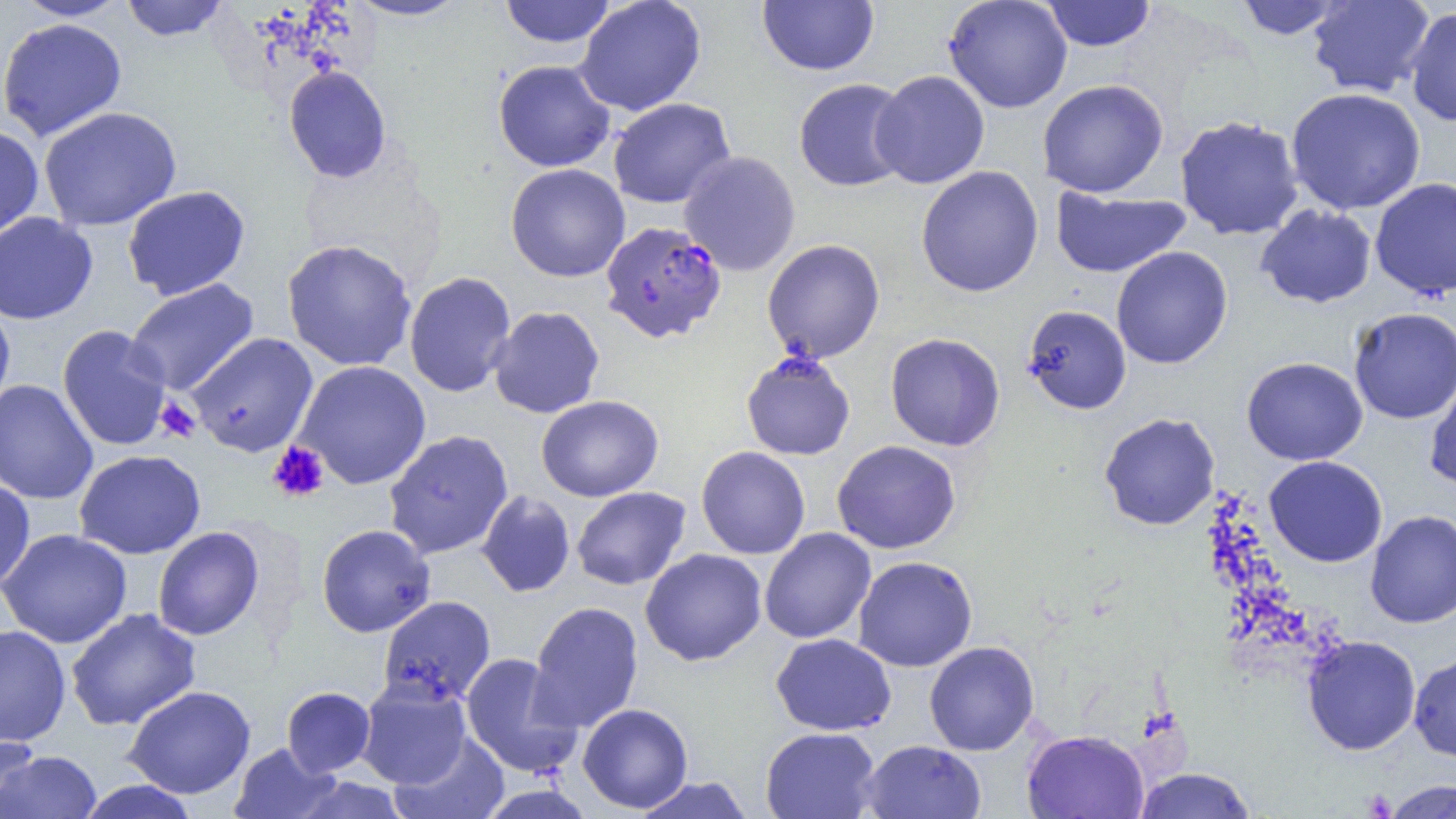

slide-level diagnosis = Plasmodium falciparum
field of view = one of a larger specimen
modality = optical microscopy
Plasmodium falciparum-infected red blood cell locations = approximate bounding boxes as (x1, y1, x2, y2) in pixels: (600, 221, 727, 343)
image size = 1456×819 pixels
platelet locations = approximate bounding boxes as (x1, y1, x2, y2) in pixels: (155, 397, 201, 442), (268, 441, 330, 503), (1361, 788, 1397, 817)
uninfected red blood cell locations = approximate bounding boxes as (x1, y1, x2, y2) in pixels: (12, 0, 132, 21), (119, 0, 231, 42), (345, 0, 471, 21), (499, 0, 618, 48), (575, 0, 706, 116), (943, 0, 1073, 113), (1232, 0, 1349, 40), (1306, 0, 1434, 98), (757, 1, 879, 76), (1041, 1, 1157, 52), (1405, 6, 1456, 127), (0, 17, 127, 142), (492, 59, 616, 172), (284, 65, 391, 183), (871, 70, 990, 189), (793, 78, 912, 192), (1037, 79, 1169, 198), (1286, 88, 1426, 215), (608, 97, 735, 209), (38, 106, 182, 231), (1174, 115, 1305, 241), (0, 125, 45, 242), (678, 151, 801, 276), (505, 163, 630, 282), (915, 166, 1044, 297), (1370, 177, 1456, 300), (122, 185, 251, 300), (1050, 188, 1191, 278), (1255, 204, 1377, 308), (0, 212, 98, 325), (281, 238, 417, 372), (762, 239, 885, 363), (1111, 246, 1233, 369), (403, 271, 517, 398), (124, 278, 260, 397), (1022, 304, 1132, 415), (0, 305, 15, 413), (488, 306, 605, 418), (1348, 307, 1456, 424), (57, 325, 172, 451), (186, 332, 319, 458), (885, 333, 1006, 451), (741, 352, 855, 460), (1241, 357, 1368, 465), (293, 360, 431, 490), (1424, 372, 1456, 490), (0, 379, 99, 505), (536, 395, 663, 502), (1099, 411, 1220, 530), (383, 430, 514, 560), (832, 440, 961, 554), (696, 446, 811, 559), (74, 450, 206, 559), (1264, 455, 1388, 567), (0, 480, 36, 592), (571, 486, 691, 590), (476, 490, 576, 597), (1365, 510, 1456, 628), (316, 523, 436, 637), (152, 526, 265, 641), (0, 528, 132, 648), (759, 528, 876, 644), (640, 548, 767, 666), (852, 556, 977, 672), (378, 595, 496, 706), (528, 601, 644, 732), (65, 607, 202, 731), (0, 625, 71, 746), (770, 633, 897, 736), (1302, 635, 1421, 755), (924, 641, 1039, 755), (460, 653, 582, 778), (1409, 653, 1456, 761), (356, 678, 472, 789), (123, 685, 256, 799), (282, 686, 376, 777), (577, 703, 693, 813), (760, 726, 881, 819), (1022, 729, 1149, 819), (391, 732, 510, 819), (0, 734, 42, 817), (859, 740, 987, 819), (229, 742, 340, 819), (2, 750, 102, 818), (1133, 767, 1257, 819), (631, 776, 756, 819), (1381, 778, 1456, 819), (76, 779, 203, 819)
preparation = thin blood smear
magnification = 1000x